Classify this cell by malaria status.
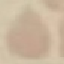
It is uninfected.

Summary:
  - Stain: Giemsa
  - Capture: smartphone through the microscope eyepiece
  - Image type: cell patch, automatically extracted from a larger field of view and resized to 64 × 64 pixels
  - Preparation: thin blood film